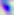
Summary:
  - Magnification: 400x
  - Identification: Toxoplasma gondii
  - Modality: photomicrograph